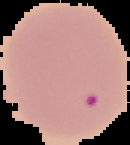

{
  "result": "no malaria parasites detected",
  "image_size": "130×145 pixels",
  "image_type": "segmented cell region on a black background",
  "preparation": "thin blood film"
}